Classify this cell by malaria status.
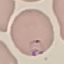
Parasitized.

capture = smartphone through the microscope eyepiece
stain = Giemsa
image type = cell patch, automatically extracted from a larger field of view and resized to 64 × 64 pixels
preparation = thin blood film